Assess this cell for malaria.
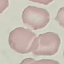

It is uninfected.

Thin smear of blood. Photographed with a smartphone camera at the microscope eyepiece. Giemsa stain. Cell patch, automatically extracted from a larger field of view and resized to 64 × 64 pixels.